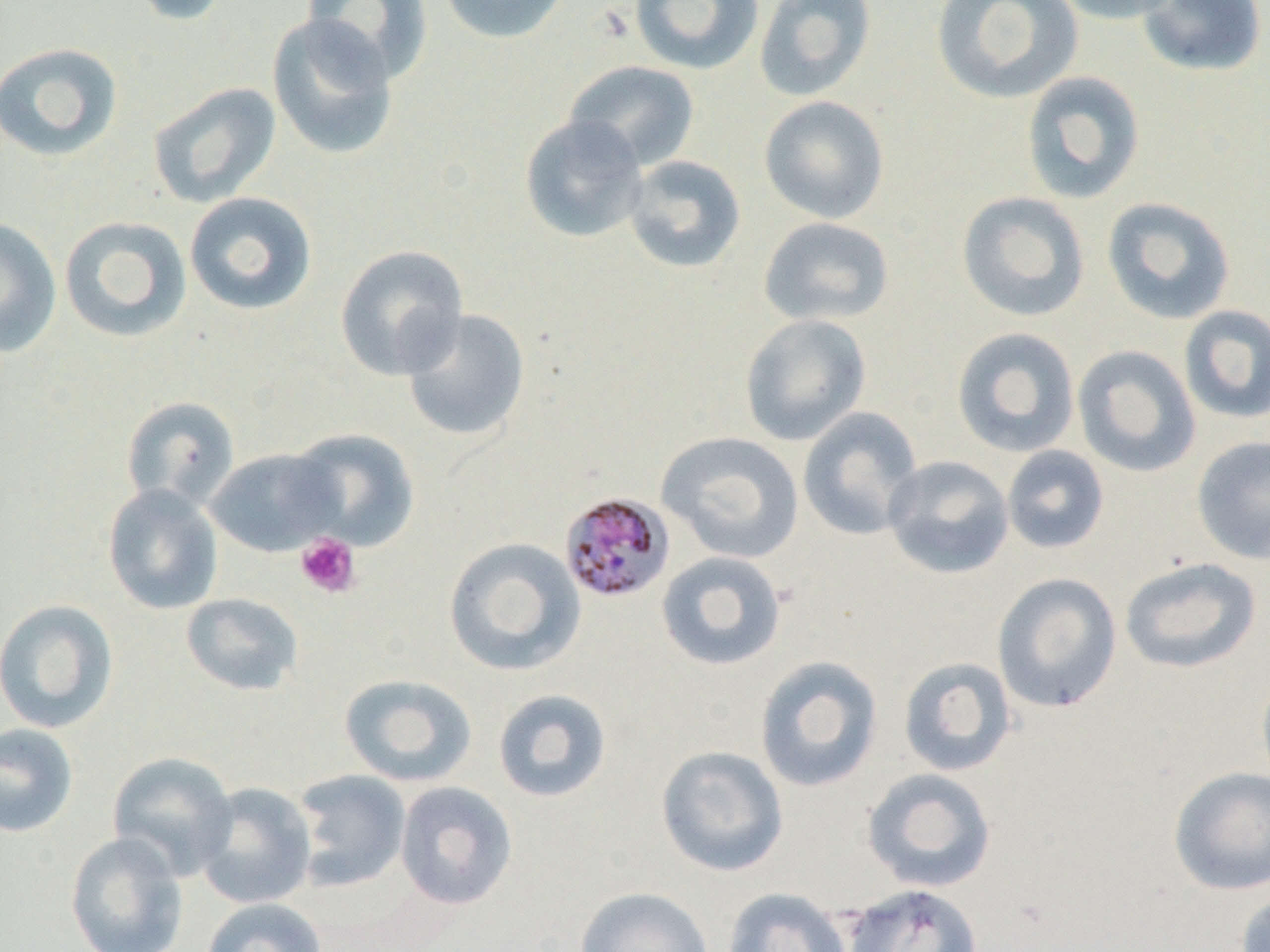

Summary:
  - Coordinate format: approximate bounding boxes as (x1, y1, x2, y2) in pixels
  - Uninfected red blood cell locations: (128, 0, 234, 26), (302, 0, 433, 84), (438, 0, 571, 44), (629, 0, 763, 74), (754, 0, 877, 101), (930, 0, 1084, 104), (1048, 0, 1185, 24), (1137, 0, 1267, 77), (268, 13, 399, 160), (0, 42, 124, 162), (563, 60, 700, 171), (1020, 71, 1146, 204), (147, 82, 282, 208), (759, 95, 889, 223), (519, 114, 649, 243), (623, 154, 746, 274), (184, 191, 318, 316), (956, 191, 1091, 322), (1101, 196, 1237, 325), (59, 216, 192, 343), (758, 216, 895, 327), (0, 219, 62, 357), (335, 244, 469, 380), (1178, 304, 1270, 424), (401, 308, 531, 442), (739, 313, 872, 446), (951, 327, 1080, 458), (1072, 345, 1202, 478), (121, 396, 240, 510), (797, 406, 924, 541), (285, 428, 420, 551), (656, 431, 804, 564), (1191, 435, 1270, 565), (1002, 445, 1109, 554), (205, 448, 343, 557), (882, 454, 1014, 579), (102, 484, 223, 615), (443, 537, 586, 676), (655, 551, 787, 671), (1120, 557, 1262, 674), (992, 572, 1122, 713), (181, 592, 304, 696), (0, 599, 119, 734), (754, 655, 883, 792), (898, 657, 1017, 777), (1256, 670, 1270, 790), (339, 674, 478, 787), (492, 688, 612, 803), (0, 723, 79, 838), (656, 744, 789, 877), (107, 751, 239, 881), (1168, 766, 1270, 895), (861, 767, 997, 893), (292, 769, 411, 891), (194, 781, 317, 909), (394, 781, 517, 910), (65, 832, 189, 952), (842, 883, 984, 952), (574, 886, 714, 952), (722, 888, 853, 952), (1235, 890, 1270, 952), (201, 897, 328, 952)
  - Platelet locations: (296, 532, 361, 598)
  - Plasmodium malariae-infected red blood cell locations: (559, 492, 676, 604)
  - Slide-level diagnosis: Plasmodium malariae
  - Modality: optical microscopy
  - Field of view: one of a larger specimen
  - Image size: 1270×952 pixels
  - Magnification: 1000x
  - Preparation: thin blood film